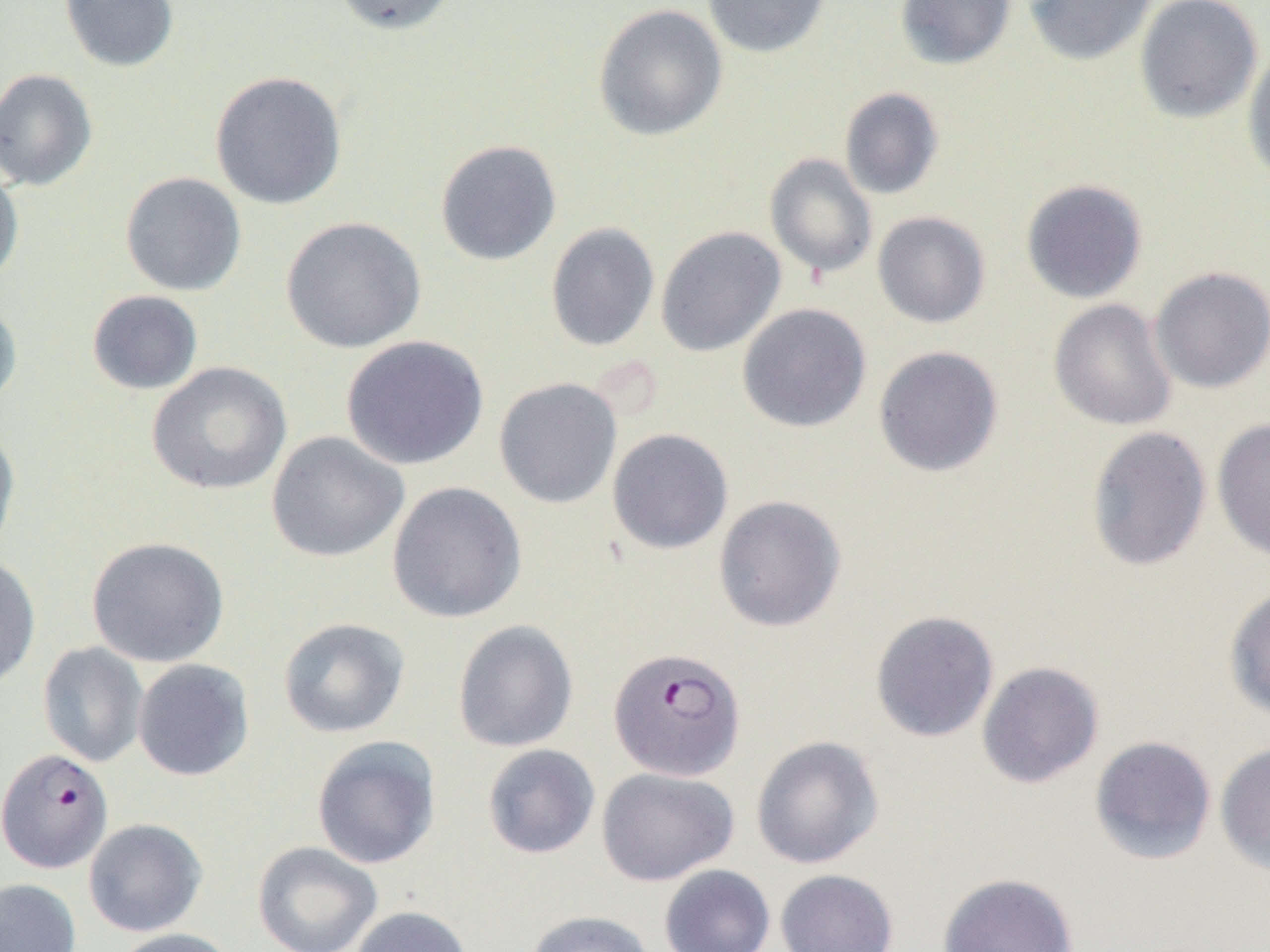
Approximate bounding boxes as (x1, y1, x2, y2) in pixels. Plasmodium falciparum-infected red blood cell locations: (608, 646, 746, 781), (0, 748, 113, 874). Uninfected red blood cell locations: (59, 0, 179, 72), (330, 0, 458, 36), (702, 0, 832, 58), (895, 0, 1016, 70), (1024, 0, 1157, 66), (1134, 0, 1263, 124), (593, 3, 728, 141), (1242, 46, 1270, 188), (0, 68, 98, 191), (210, 71, 347, 210), (839, 87, 944, 200), (434, 139, 562, 266), (764, 153, 878, 279), (0, 165, 24, 286), (120, 172, 247, 296), (1020, 179, 1148, 303), (873, 211, 991, 328), (280, 216, 426, 353), (545, 222, 659, 352), (655, 226, 786, 356), (1150, 266, 1270, 393), (86, 290, 203, 395), (0, 297, 22, 411), (1048, 299, 1178, 431), (737, 302, 871, 433), (341, 335, 489, 470), (873, 345, 1004, 477), (147, 361, 292, 496), (494, 377, 623, 509), (1212, 417, 1270, 562), (0, 425, 21, 560), (1085, 426, 1212, 572), (607, 428, 734, 555), (266, 431, 409, 563), (386, 481, 527, 623), (712, 495, 847, 632), (86, 536, 228, 667), (0, 553, 41, 691), (1223, 584, 1270, 722), (870, 609, 999, 742), (278, 617, 410, 738), (452, 620, 579, 753), (38, 641, 148, 767), (133, 659, 254, 781), (976, 660, 1104, 789), (750, 735, 884, 869), (1089, 735, 1217, 865), (311, 736, 441, 869), (1214, 743, 1270, 876), (482, 744, 601, 859), (596, 767, 739, 886), (83, 818, 208, 937), (252, 841, 383, 952), (658, 864, 775, 952), (775, 869, 899, 952), (937, 872, 1079, 952), (0, 878, 82, 952), (349, 905, 474, 952), (523, 910, 657, 952), (111, 927, 239, 952). Slide-level diagnosis: Plasmodium falciparum. Thin blood film. 1000x magnification. One field of a larger specimen. Light microscopy. Image is 1270×952 pixels.